State the blood parasite species.
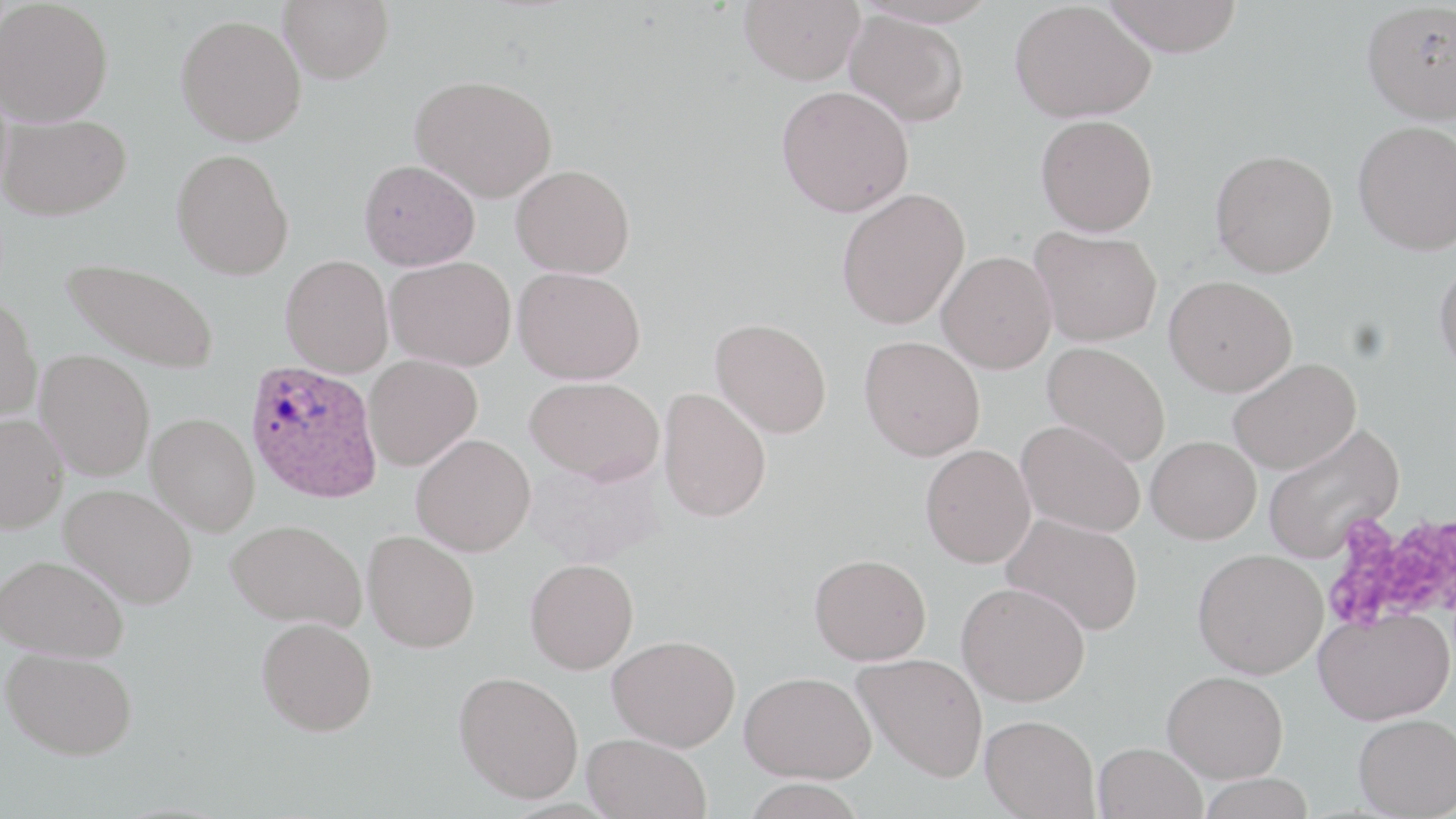

Plasmodium ovale.

uninfected red blood cell locations = approximate bounding boxes as (x1, y1, x2, y2) in pixels: (279, 0, 394, 83), (738, 0, 865, 85), (1101, 0, 1244, 57), (0, 1, 113, 127), (1009, 1, 1155, 123), (1362, 2, 1456, 124), (844, 10, 969, 126), (176, 14, 306, 146), (411, 74, 558, 202), (776, 86, 914, 216), (0, 113, 132, 220), (1036, 114, 1158, 236), (1353, 120, 1456, 255), (1210, 148, 1339, 278), (171, 149, 294, 280), (359, 159, 480, 270), (511, 165, 635, 278), (836, 187, 970, 329), (1031, 227, 1162, 346), (936, 251, 1056, 373), (281, 254, 393, 377), (61, 256, 220, 374), (385, 256, 516, 371), (1434, 257, 1456, 378), (514, 266, 645, 384), (1164, 275, 1297, 396), (0, 293, 43, 424), (710, 318, 832, 438), (859, 335, 985, 460), (1042, 342, 1170, 466), (35, 350, 155, 480), (363, 355, 482, 470), (1227, 357, 1361, 474), (525, 377, 665, 484), (658, 387, 772, 522), (147, 412, 259, 536), (0, 414, 68, 533), (1016, 420, 1145, 536), (1262, 423, 1405, 563), (411, 433, 536, 556), (1145, 435, 1261, 544), (921, 444, 1036, 568), (527, 456, 665, 568), (59, 483, 197, 608), (1001, 513, 1143, 636), (226, 518, 366, 630), (362, 530, 480, 653), (1193, 548, 1328, 678), (0, 553, 129, 662), (809, 553, 931, 665), (525, 558, 639, 674), (957, 581, 1090, 706), (1314, 607, 1454, 725), (256, 617, 377, 736), (608, 634, 740, 750), (1, 647, 138, 760), (852, 652, 988, 781), (740, 670, 876, 783), (1163, 670, 1288, 782), (453, 671, 584, 803), (1353, 713, 1456, 818), (980, 715, 1100, 818), (584, 733, 711, 819), (1094, 742, 1207, 819), (1197, 774, 1316, 818), (740, 778, 869, 819)
Plasmodium ovale-infected red blood cell locations = approximate bounding boxes as (x1, y1, x2, y2) in pixels: (245, 359, 383, 503)
magnification = 1000x
image size = 1456×819 pixels
field of view = single
stain = May-Grünwald-Giemsa
preparation = thin blood smear
modality = optical microscopy
platelet locations = approximate bounding boxes as (x1, y1, x2, y2) in pixels: (1324, 507, 1454, 633)